Locate and identify every blood parasite.
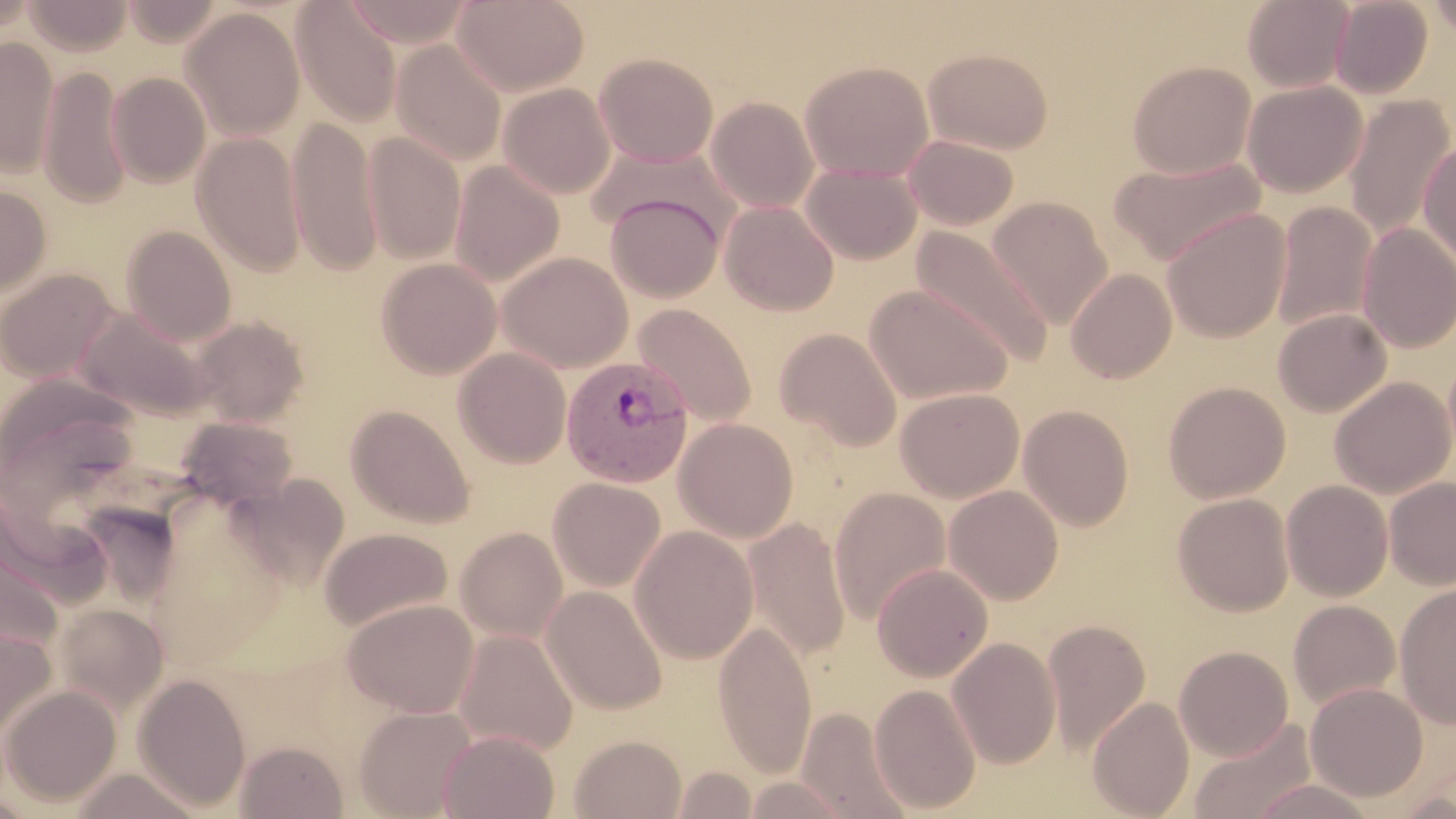
Approximate bounding boxes as [x1, y1, x2, y2] in pixels.
Plasmodium vivax-infected red blood cells: [561, 356, 694, 487].
No Plasmodium falciparum, Plasmodium ovale, Plasmodium malariae, Babesia divergens, or Trypanosoma brucei observed.

Summary:
  - Uninfected red blood cell locations: [0, 0, 38, 36], [23, 0, 133, 56], [123, 0, 225, 45], [453, 0, 589, 97], [1242, 0, 1354, 92], [1329, 0, 1433, 98], [1427, 0, 1456, 39], [341, 1, 475, 48], [292, 2, 403, 126], [180, 7, 306, 142], [0, 36, 59, 177], [390, 39, 507, 166], [923, 47, 1054, 155], [594, 53, 718, 168], [799, 60, 934, 182], [1127, 60, 1256, 179], [38, 65, 131, 209], [107, 71, 211, 188], [1243, 80, 1367, 197], [498, 83, 616, 199], [1343, 95, 1455, 241], [705, 96, 819, 214], [287, 116, 382, 277], [362, 131, 466, 264], [191, 132, 307, 276], [903, 133, 1019, 230], [1418, 138, 1456, 269], [1107, 154, 1267, 267], [449, 160, 564, 286], [801, 163, 922, 264], [0, 185, 52, 299], [605, 191, 725, 303], [986, 196, 1113, 330], [719, 200, 839, 316], [1271, 202, 1376, 332], [1162, 208, 1291, 343], [1357, 223, 1456, 353], [121, 225, 236, 345], [911, 225, 1054, 368], [498, 251, 633, 372], [376, 257, 501, 379], [0, 268, 118, 383], [1066, 268, 1177, 383], [864, 284, 1013, 404], [631, 303, 757, 428], [74, 306, 212, 420], [1272, 309, 1391, 417], [190, 316, 309, 427], [775, 328, 902, 450], [453, 347, 572, 468], [1, 376, 141, 510], [1330, 376, 1455, 498], [1163, 381, 1290, 503], [895, 387, 1024, 502], [346, 404, 475, 529], [1018, 404, 1135, 532], [175, 417, 299, 510], [674, 418, 798, 543], [230, 474, 350, 590], [1384, 476, 1455, 589], [547, 477, 666, 592], [1281, 480, 1393, 601], [944, 485, 1064, 605], [829, 487, 951, 624], [1173, 493, 1294, 616], [743, 517, 851, 663], [629, 525, 758, 664], [319, 526, 453, 632], [455, 526, 568, 643], [0, 542, 63, 661], [871, 562, 993, 682], [1394, 583, 1456, 728], [541, 585, 667, 715], [343, 598, 479, 717], [1288, 600, 1401, 710], [54, 604, 168, 715], [714, 619, 816, 777], [1042, 619, 1151, 754], [0, 626, 58, 742], [453, 629, 578, 755], [947, 636, 1062, 769], [1174, 645, 1294, 761], [133, 672, 252, 812], [1305, 682, 1428, 802], [869, 683, 981, 815], [1, 684, 121, 808], [1087, 696, 1195, 818], [353, 704, 478, 818], [796, 705, 913, 817], [1188, 718, 1318, 819], [438, 729, 560, 818], [569, 734, 687, 818], [236, 740, 348, 819], [671, 765, 758, 819], [66, 768, 204, 818], [741, 776, 851, 818], [1246, 777, 1378, 818]
  - Slide-level diagnosis: Plasmodium vivax
  - Image size: 1456×819 pixels
  - Modality: light microscopy
  - Field of view: single
  - Magnification: 1000x
  - Stain: May-Grünwald-Giemsa
  - Preparation: thin blood film